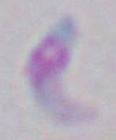
identification = Toxoplasma gondii
magnification = 1000x
modality = micrograph